Classify the preparation.
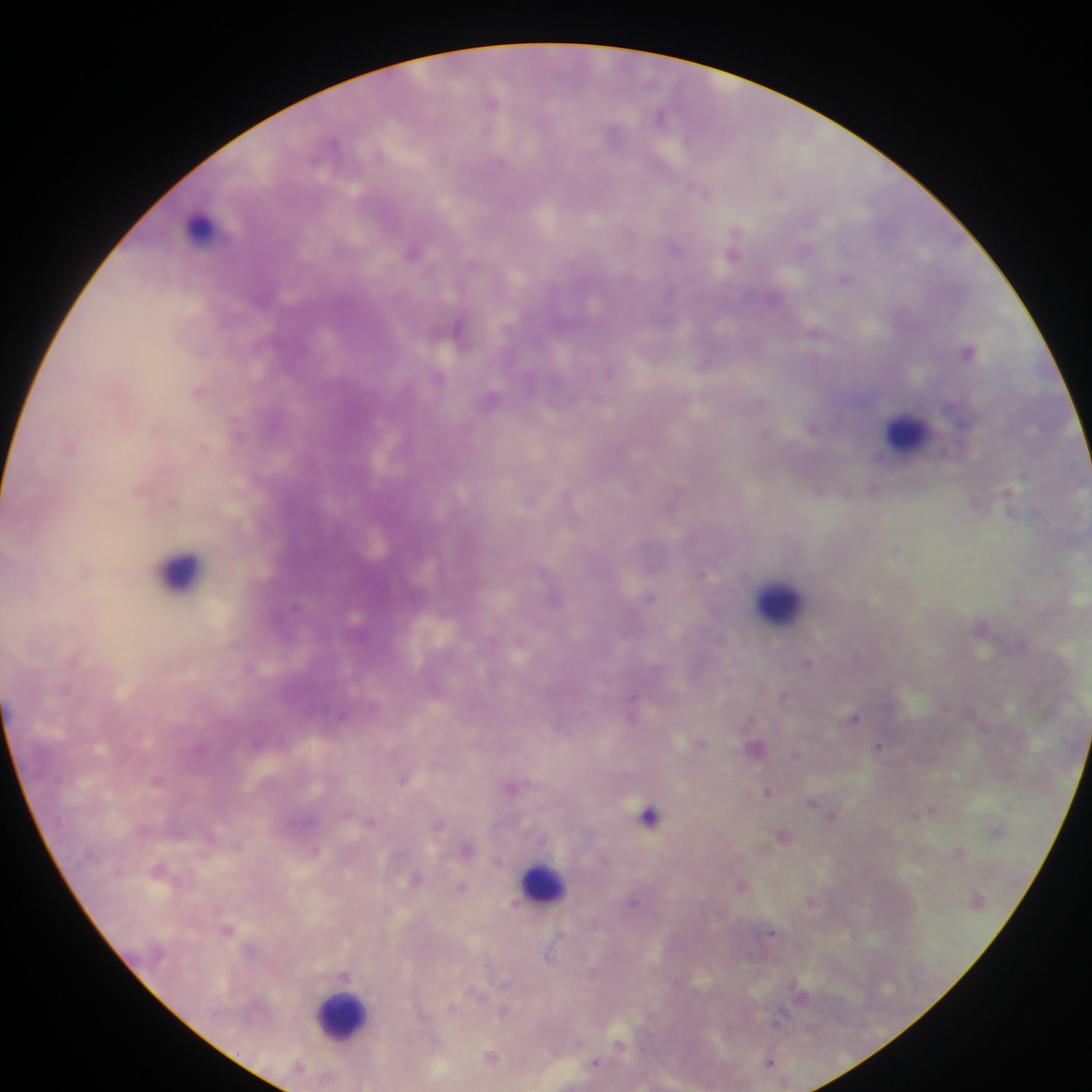

Thick blood film.

Approximate centers as x y in pixels.
Summary:
  - Leukocyte locations: 201 228; 906 433; 180 572; 778 602; 543 882; 341 1017
  - Malaria parasite locations: 495 100; 661 115; 500 160; 701 188; 735 251; 413 252; 845 278; 773 298; 459 328; 816 333; 201 350; 969 351; 703 366; 441 377; 200 391; 494 397; 237 426; 813 428; 72 445; 820 489; 874 489; 140 490; 1009 496; 569 498; 531 500; 976 500; 174 501; 896 550; 85 570; 704 573; 650 598; 294 607; 521 643; 808 662; 250 668; 785 697; 633 705; 946 706; 342 715; 854 716; 700 743; 880 746; 755 747; 796 755; 404 779; 157 780; 512 787; 768 791; 816 804; 931 810; 831 813; 649 815; 371 821; 439 825; 784 835; 237 846; 468 848; 316 850; 960 851; 605 858; 499 860; 159 870; 416 879; 742 885; 462 886; 634 901; 812 901; 515 903; 228 929; 773 932; 550 952; 594 974; 344 975; 799 992; 453 1007; 504 1010; 620 1045; 493 1057; 770 1061; 596 1062
  - Image size: 1092×1092 pixels
  - Country: Ghana
  - Field of view: single
  - Capture: mobile-phone photograph through a microscope